Name the parasite shown.
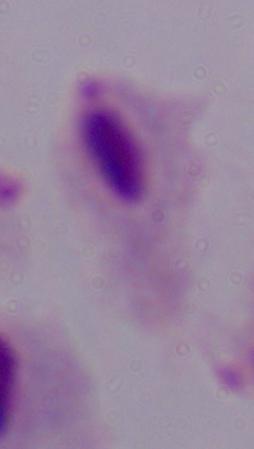

This is a trichomonad.

1000x magnification. Photomicrograph.